Assess this cell for malaria.
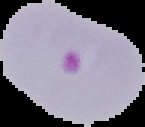
Parasitized.

preparation = thin blood film
image size = 145×127 pixels
image type = segmented cell region on a black background